Classify this cell by malaria status.
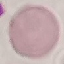
It is uninfected.

Summary:
  - Stain: Giemsa
  - Capture: smartphone through the microscope eyepiece
  - Preparation: thin blood film
  - Image type: automatically extracted cell patch, resized to 64 × 64 pixels